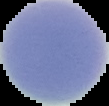

Summary:
  - Image type: segmented cell region on a black background
  - Preparation: thin blood film
  - Result: negative for malaria parasites
  - Image size: 109×106 pixels